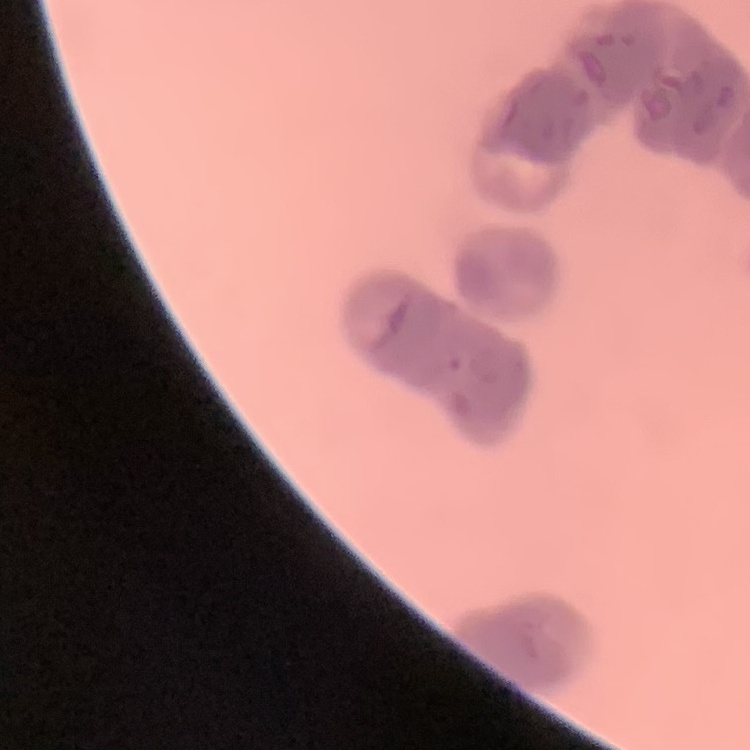
The erythrocytes show rouleaux formation. Square crop of a larger photomicrograph. Thin blood smear. Field's or Giemsa stain.